Report the malaria status of this cell.
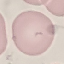

Uninfected.

Giemsa stain. Cell patch, automatically extracted from a larger field of view and resized to 64 × 64 pixels. Thin smear of blood. Photographed with a smartphone camera at the microscope eyepiece.